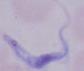

Summary:
  - Identification: trypanosome
  - Modality: micrograph
  - Magnification: 1000x